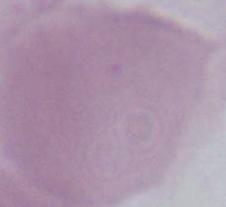
identification = red blood cell
magnification = 1000x
modality = micrograph